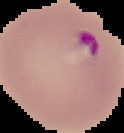 From a thin blood film. Result: malaria parasites identified. Image is 124×133 pixels. Segmented cell region on a black background.